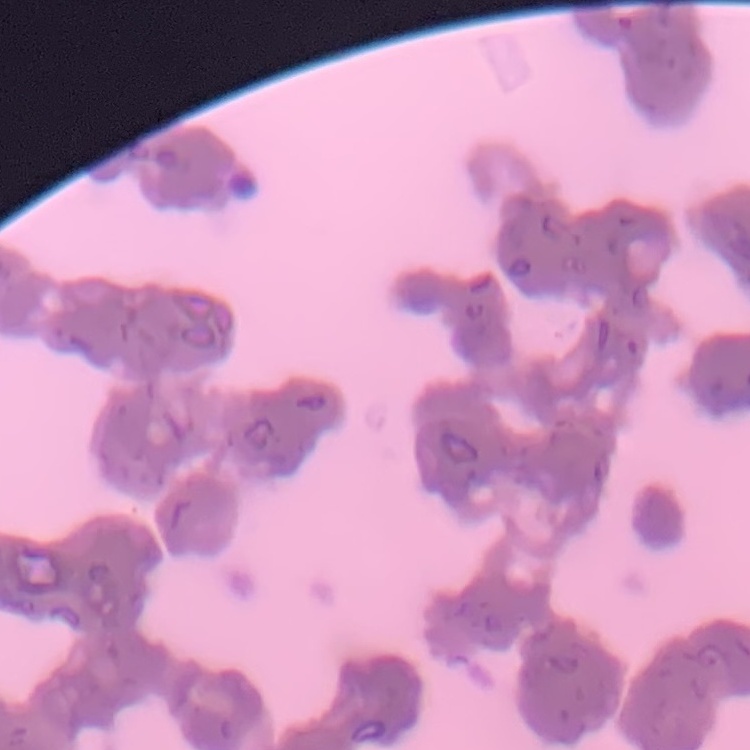

Summary:
  - Erythrocyte morphology: rouleaux formation
  - Preparation: thin blood film
  - Image type: square crop of a larger photomicrograph
  - Stain: Field's or Giemsa